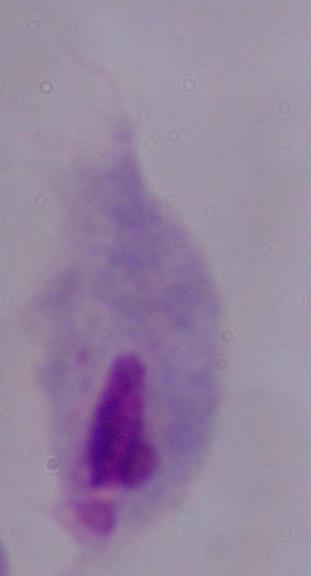
Summary:
  - Identification: trichomonad
  - Modality: micrograph
  - Magnification: 1000x